State which cell type is depicted.
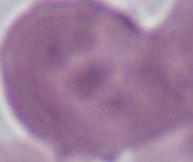

This is an erythrocyte.

Micrograph. 1000x magnification.